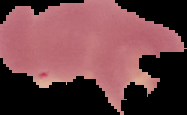

{
  "preparation": "thin blood film",
  "image_size": "187×115 pixels",
  "image_type": "segmented cell region on a black background",
  "malaria_status": "uninfected"
}